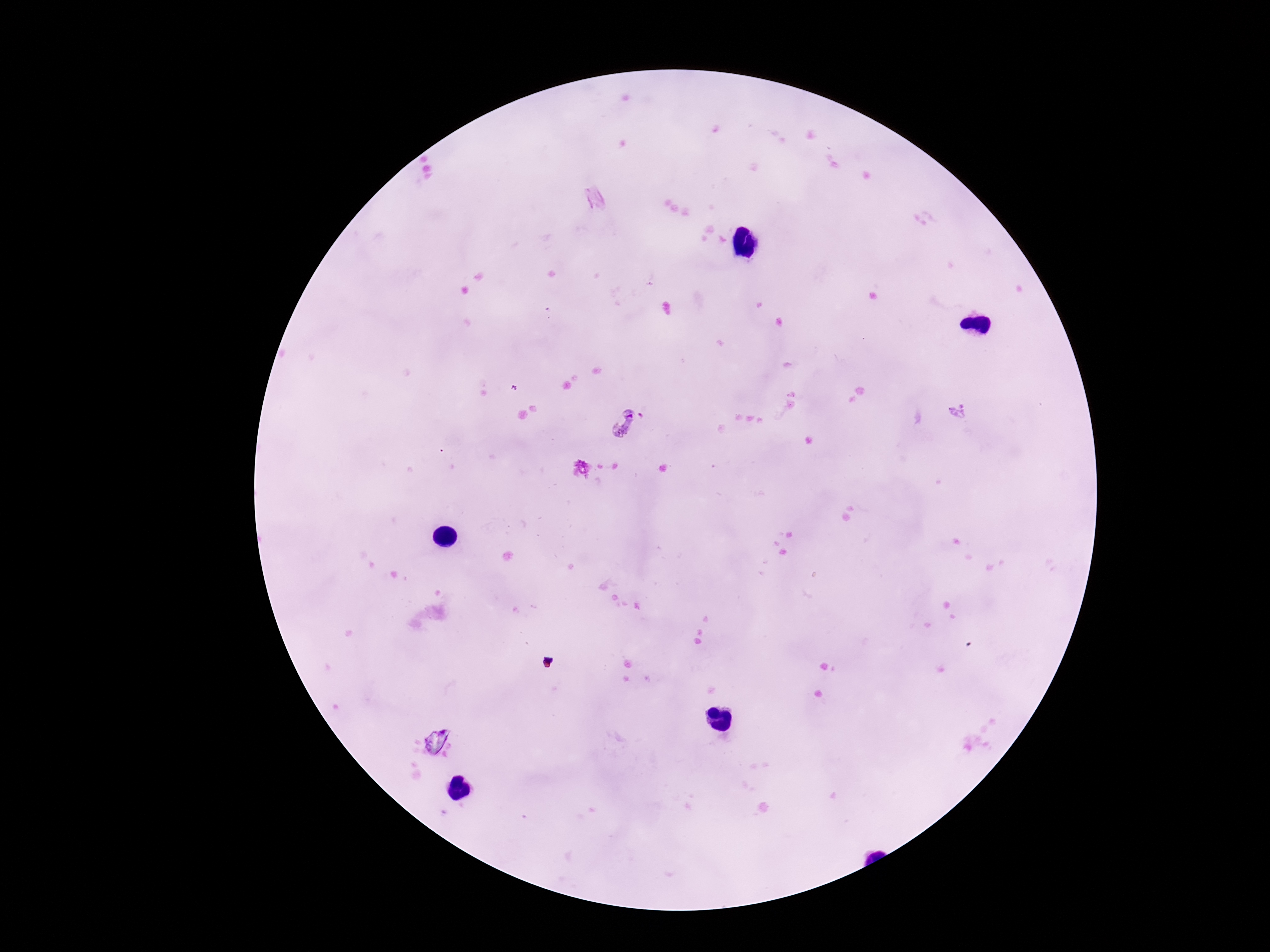
{
  "patient_malaria_status": "positive",
  "stain": "Giemsa",
  "magnification": "100x",
  "plasmodium_parasite_locations": "approximate centers as [x, y] in pixels: [957, 410], [624, 423]",
  "capture": "smartphone camera through the microscope eyepiece",
  "field_of_view": "one from this slide",
  "image_size": "1270×952 pixels",
  "preparation": "thick peripheral-blood smear"
}